Assess the morphology of the erythrocytes.
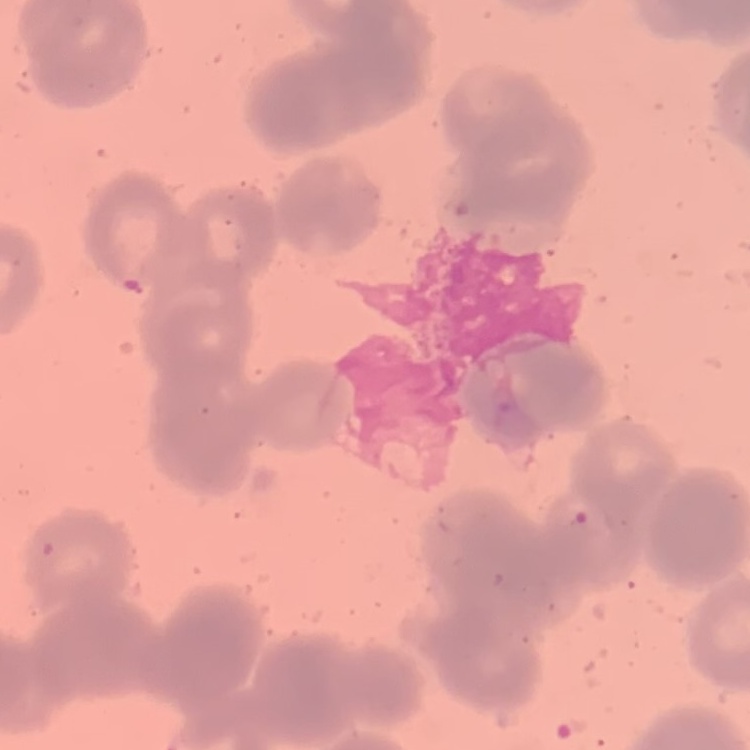
They show rouleaux formation.

preparation = thin blood film
image type = one tile cut from a larger photomicrograph
stain = Field's or Giemsa